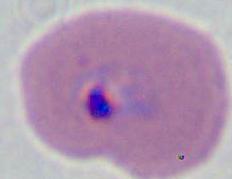
Photomicrograph. Captured at either 400x or 1000x magnification. A Plasmodium parasite is shown.